Outline each blood parasite and name the species.
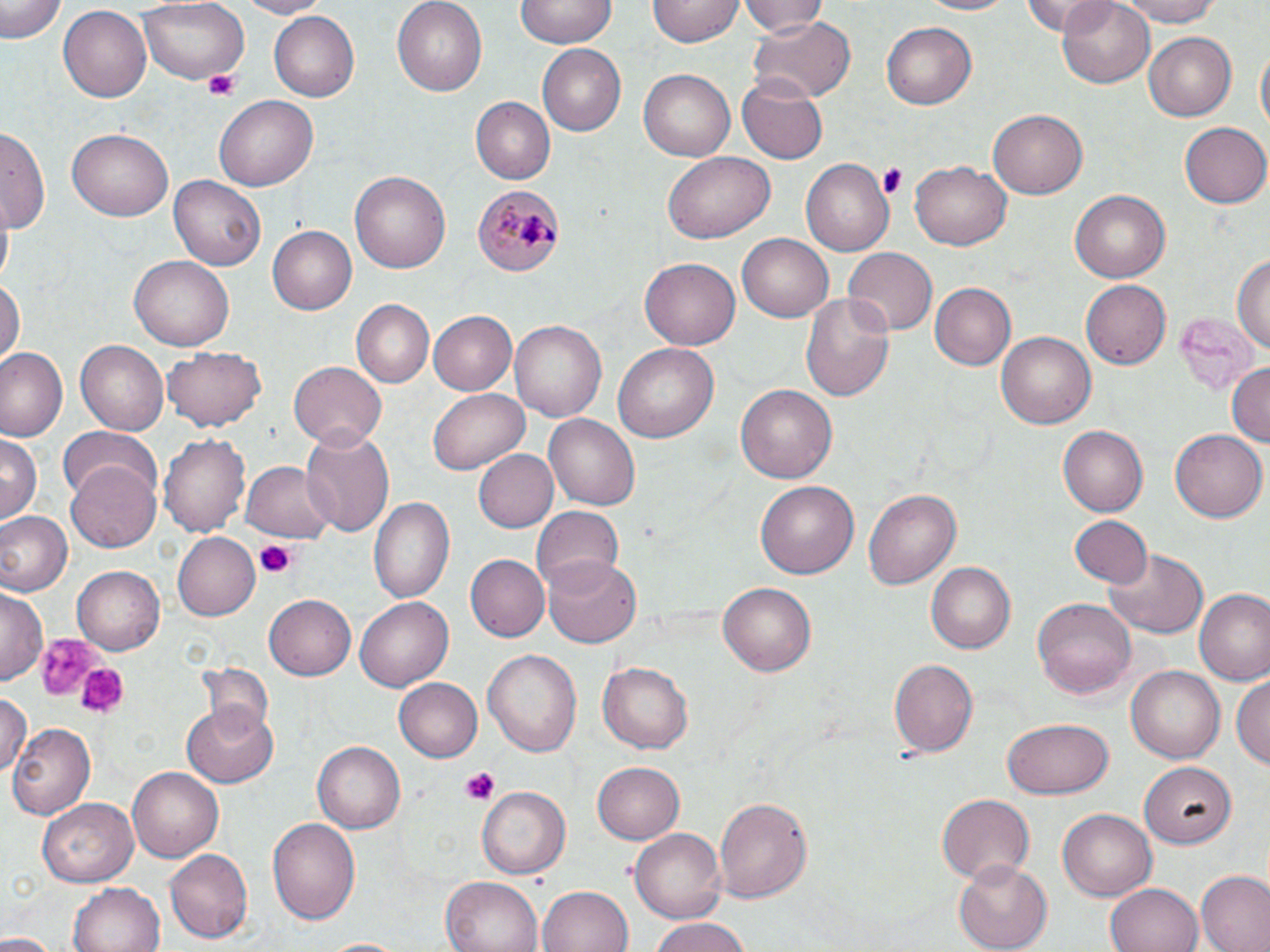
Approximate bounding boxes as (x1, y1, x2, y2) in pixels.
Plasmodium malariae-infected red blood cells: (476, 182, 564, 280).
No Plasmodium falciparum, Plasmodium ovale, Plasmodium vivax, Babesia divergens, or Trypanosoma brucei observed.

slide-level diagnosis = Plasmodium malariae
stain = May-Grünwald-Giemsa
platelet locations = approximate bounding boxes as (x1, y1, x2, y2) in pixels: (203, 69, 242, 100), (879, 162, 908, 198), (255, 540, 299, 580), (33, 631, 100, 703), (74, 659, 125, 719), (459, 767, 500, 806)
image size = 1270×952 pixels
uninfected red blood cell locations = approximate bounding boxes as (x1, y1, x2, y2) in pixels: (0, 0, 63, 44), (230, 0, 329, 18), (390, 0, 487, 92), (516, 0, 615, 49), (741, 0, 828, 41), (910, 0, 1019, 16), (1021, 0, 1121, 35), (1110, 0, 1227, 26), (139, 1, 249, 84), (648, 1, 742, 47), (1055, 2, 1156, 87), (57, 7, 149, 103), (268, 11, 361, 101), (747, 16, 853, 105), (882, 22, 977, 111), (1143, 32, 1241, 118), (535, 44, 624, 135), (1255, 44, 1269, 144), (639, 69, 736, 161), (739, 76, 827, 163), (214, 96, 318, 191), (470, 97, 555, 184), (988, 109, 1089, 199), (1181, 121, 1270, 208), (67, 124, 173, 217), (0, 128, 47, 230), (664, 150, 774, 243), (911, 157, 1012, 248), (802, 160, 893, 255), (350, 171, 451, 274), (168, 173, 267, 273), (1069, 190, 1168, 283), (266, 223, 357, 313), (737, 234, 832, 322), (843, 248, 935, 338), (1231, 253, 1270, 350), (131, 254, 233, 347), (639, 259, 741, 350), (0, 279, 23, 367), (1082, 279, 1170, 369), (930, 283, 1017, 371), (800, 289, 895, 404), (351, 300, 432, 387), (1174, 303, 1259, 450), (428, 311, 516, 394), (511, 319, 606, 423), (994, 329, 1097, 432), (74, 340, 169, 435), (611, 342, 720, 446), (0, 347, 66, 441), (162, 347, 267, 430), (291, 360, 386, 450), (1227, 362, 1269, 453), (735, 384, 837, 484), (427, 386, 528, 476), (543, 415, 642, 509), (57, 424, 163, 509), (1057, 425, 1147, 517), (1170, 429, 1267, 524), (300, 430, 396, 538), (161, 432, 252, 538), (0, 433, 41, 521), (472, 448, 558, 532), (241, 458, 337, 544), (68, 465, 161, 552), (755, 479, 859, 580), (863, 485, 961, 587), (370, 495, 456, 605), (533, 506, 625, 590), (1, 511, 71, 595), (1068, 515, 1152, 589), (171, 531, 260, 621), (1104, 545, 1209, 638), (465, 554, 550, 641), (544, 559, 643, 648), (926, 563, 1015, 654), (72, 566, 165, 655), (719, 582, 815, 676), (1193, 588, 1269, 684), (0, 590, 45, 685), (265, 595, 356, 681), (1031, 595, 1137, 702), (355, 596, 452, 691), (482, 646, 582, 756), (887, 658, 977, 758), (597, 661, 692, 754), (1126, 664, 1226, 764), (1234, 673, 1269, 774), (392, 676, 483, 762), (0, 694, 28, 780), (181, 700, 279, 787), (1001, 717, 1113, 799), (9, 722, 95, 821), (312, 741, 403, 833), (591, 761, 686, 845), (1143, 762, 1234, 851), (128, 766, 227, 863), (475, 786, 568, 880), (935, 793, 1036, 882), (38, 795, 138, 885), (714, 796, 813, 903), (1056, 808, 1157, 902), (266, 816, 361, 927), (629, 826, 727, 924), (166, 849, 252, 943), (955, 861, 1052, 950), (1197, 872, 1270, 952), (441, 876, 545, 952), (69, 880, 164, 952), (1105, 882, 1201, 952), (538, 885, 634, 952), (646, 917, 755, 952), (0, 933, 58, 952), (319, 938, 409, 952)
magnification = 1000x
modality = light microscopy
field of view = one of a larger specimen
preparation = thin blood film